Report the malaria status of this cell.
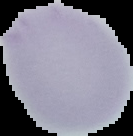

Uninfected.

Summary:
  - Image type: segmented cell region with the area outside set to black
  - Preparation: thin blood smear
  - Image size: 133×136 pixels